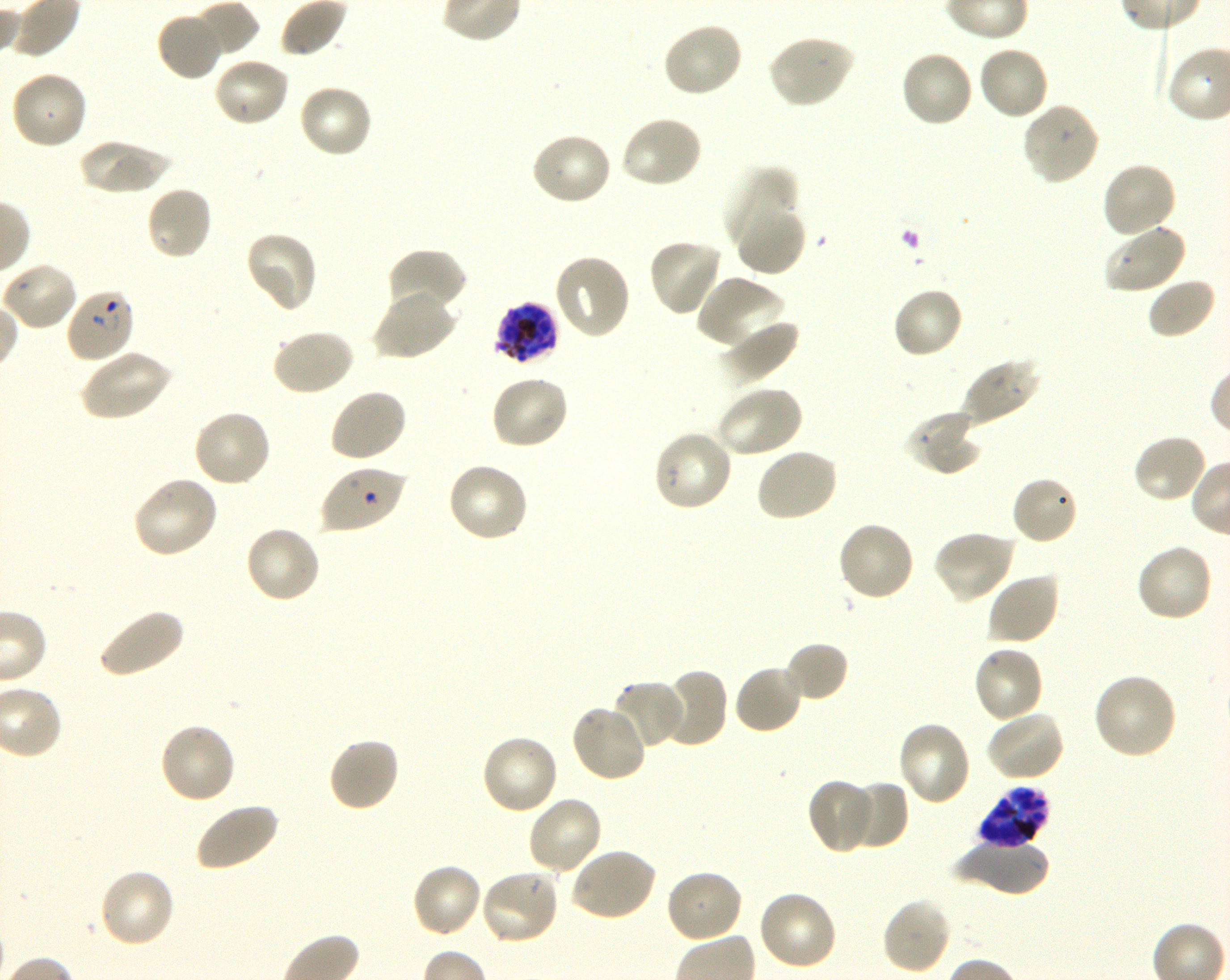
Approximate bounding boxes as (x1, y1, x2, y2) in pixels. Not every red blood cell is marked. A life-cycle stage — or a range of stages, where the recorded stages span more than one — follows each staged infected red blood cell. Locations of red blood cells of indeterminate infection status: (320, 465, 407, 534). Locations of uninfected red blood cells: (191, 0, 259, 59), (156, 12, 223, 81), (661, 21, 745, 99), (767, 34, 855, 110), (977, 44, 1050, 121), (899, 49, 974, 128), (212, 57, 290, 128), (10, 71, 88, 152), (297, 83, 374, 159), (1021, 102, 1102, 186), (619, 114, 703, 190), (530, 132, 613, 207), (77, 138, 173, 194), (1101, 161, 1178, 240), (723, 166, 800, 252), (145, 185, 214, 261), (736, 204, 807, 278), (1104, 224, 1187, 295), (244, 230, 319, 314), (646, 237, 724, 317), (386, 247, 468, 317), (553, 253, 632, 340), (2, 262, 79, 332), (695, 275, 787, 351), (1146, 276, 1217, 340), (892, 286, 964, 359), (372, 287, 458, 361), (719, 320, 800, 385), (270, 328, 355, 397), (79, 349, 171, 422), (960, 358, 1042, 426), (489, 374, 571, 452), (714, 385, 803, 460), (328, 387, 408, 464), (191, 408, 272, 489), (904, 410, 980, 476), (652, 429, 733, 513), (1132, 434, 1209, 504), (755, 447, 839, 523), (445, 462, 530, 545), (131, 475, 219, 559), (1011, 476, 1080, 546), (836, 520, 916, 603), (244, 524, 323, 604), (932, 529, 1015, 604), (1134, 542, 1213, 623), (986, 572, 1061, 646), (97, 607, 185, 679), (783, 641, 849, 704), (972, 644, 1045, 724), (733, 663, 805, 735), (654, 668, 729, 748), (1092, 672, 1179, 760), (611, 679, 687, 748), (570, 704, 649, 783), (985, 709, 1066, 782), (897, 720, 973, 807), (157, 722, 237, 805), (480, 734, 560, 816), (327, 736, 400, 813), (807, 779, 873, 854), (843, 781, 907, 851), (526, 795, 604, 877), (193, 801, 280, 873), (950, 839, 1049, 896), (568, 847, 657, 923), (409, 862, 483, 939), (97, 866, 177, 949), (479, 868, 561, 946), (664, 868, 745, 945), (755, 890, 838, 972), (880, 896, 952, 976). Locations of infected red blood cells: (64, 287, 135, 364) early ring to early trophozoite; (494, 302, 560, 366) schizont; (976, 787, 1049, 850) late trophozoite to late schizont. 100x oil-immersion objective, numerical aperture 1.30. Giemsa stain. Image is 1230×980 pixels. One field from this slide. Blood group of the donor: O+. Plasmodium falciparum strain 3D7 maintained in shaking in-vitro culture. Thin blood film.